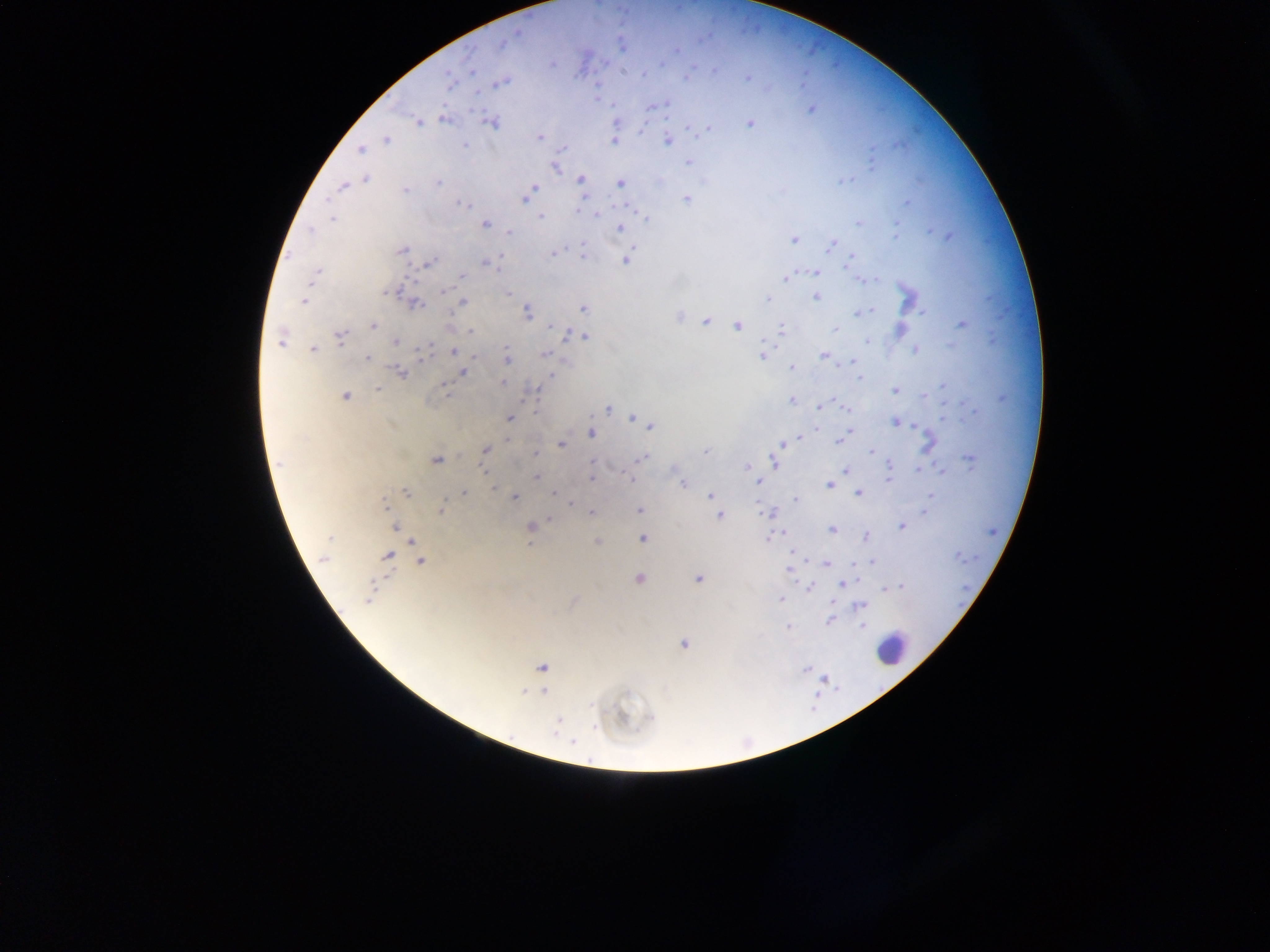

capture: mobile-phone photograph through a microscope
image_size: 1270×952 pixels
country: Ghana
leukocyte_locations: 'approximate centers as [x, y] in pixels: [891, 647]'
preparation: thick blood film
field_of_view: single
plasmodium_parasite_locations: 'approximate centers as [x, y] in pixels: [676, 51], [551, 65], [747, 76], [501, 81], [652, 106], [811, 108], [443, 118], [418, 122], [490, 122], [749, 123], [709, 128], [539, 137], [667, 139], [386, 140], [613, 141], [463, 145], [361, 149], [688, 161], [555, 166], [365, 178], [580, 179], [620, 184], [534, 186], [343, 187], [531, 190], [525, 198], [687, 198], [462, 204], [331, 217], [541, 217], [485, 224], [620, 228], [509, 233], [794, 239], [833, 244], [401, 249], [553, 252], [583, 257], [851, 257], [626, 258], [427, 262], [486, 263], [815, 272], [315, 275], [460, 275], [786, 279], [815, 296], [766, 299], [304, 301], [462, 303], [413, 304], [583, 308], [924, 312], [526, 313], [859, 313], [706, 321], [963, 323], [373, 325], [738, 326], [835, 328], [782, 329], [471, 331], [567, 335], [341, 336], [576, 336], [584, 336], [280, 339], [396, 342], [313, 349], [918, 349], [455, 351], [543, 354], [823, 355], [763, 356], [368, 359], [507, 359], [853, 361], [792, 368], [462, 371], [401, 373], [551, 375], [503, 383], [443, 386], [377, 389], [895, 391], [345, 396], [790, 400], [820, 407], [605, 408], [844, 408], [509, 418], [632, 418], [895, 422], [650, 425], [590, 432], [852, 432], [799, 438], [837, 439], [928, 443], [560, 444], [782, 445], [485, 450], [705, 451], [871, 452], [535, 455], [642, 458], [436, 459], [971, 460], [774, 462], [281, 463], [593, 463], [748, 465], [845, 470], [918, 470], [941, 471], [536, 477], [591, 479], [630, 479], [888, 480], [757, 481], [683, 484], [829, 485], [494, 488], [405, 491], [858, 492], [464, 493], [553, 493], [711, 496], [931, 496], [513, 497], [796, 500], [383, 506], [442, 509], [638, 510], [925, 512], [591, 513], [772, 513], [720, 515], [550, 518], [397, 526], [531, 526], [901, 526], [831, 529], [866, 536], [642, 538], [768, 538], [598, 542], [791, 552], [387, 555], [325, 557], [420, 560], [871, 561], [826, 564], [789, 566], [639, 578], [698, 578], [842, 584], [806, 587], [885, 589], [371, 595], [780, 599], [858, 605], [830, 621], [862, 625], [788, 628], [683, 644], [541, 667], [805, 668], [543, 691], [572, 742]'